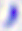
Summary:
  - Magnification: 400x
  - Identification: Toxoplasma gondii
  - Modality: photomicrograph